Draw a bounding box around every parasitised red blood cell, every trophozoite, every gametocyte, every leukocyte, and every artifact (platelet-like body, stain precipitate, or debris).
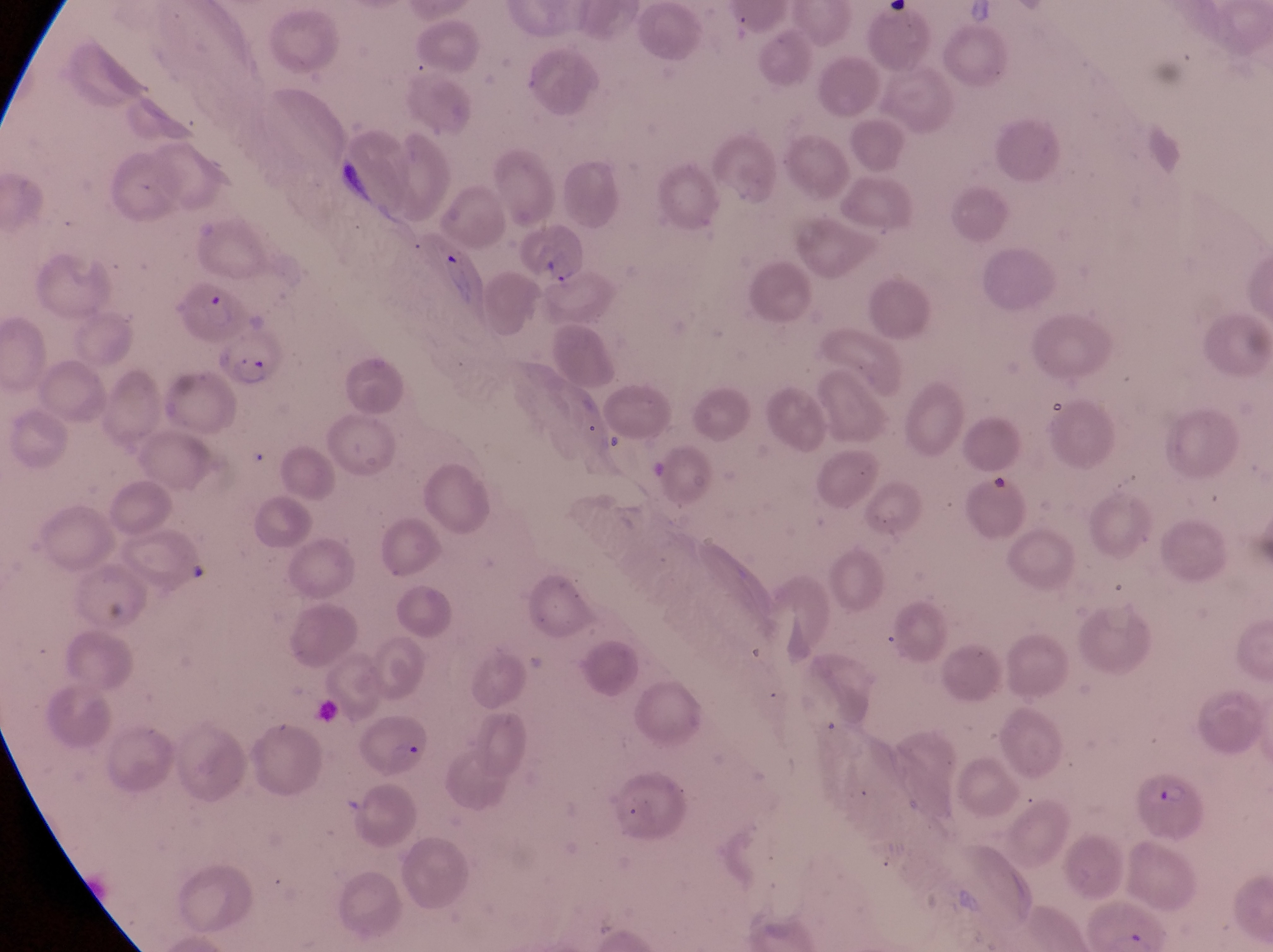
Approximate bounding boxes as (left, top, right, bottom) in pixels.
Parasitised red blood cells: (519, 225, 589, 288), (175, 283, 249, 346), (215, 334, 289, 394), (1133, 771, 1207, 845).
No leukocytes observed.
Artifacts (platelet-like body, stain precipitate, or debris): (389, 737, 426, 760).

{
  "magnification": "1000x",
  "field_of_view": "single",
  "capture": "smartphone photograph through the eyepiece of an Olympus CX-23 microscope",
  "country": "Uganda",
  "preparation": "thin blood film",
  "image_size": "1273×952 pixels"
}